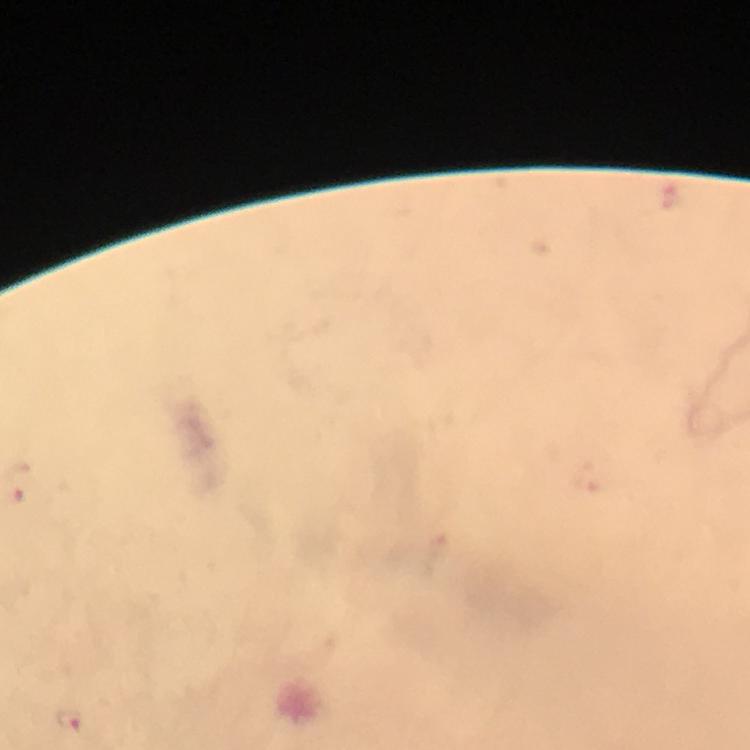

Approximate object centers, in pixels from the top-left corner. Malaria parasite locations: (x=71, y=720). At 100x magnification. Thick blood film. Giemsa-stained preparation. Immersion oil applied. From a diagnostic examination for malaria. Image is 750×750 pixels. Cropped region of a single field of view. Photographed through the microscope with a smartphone camera.